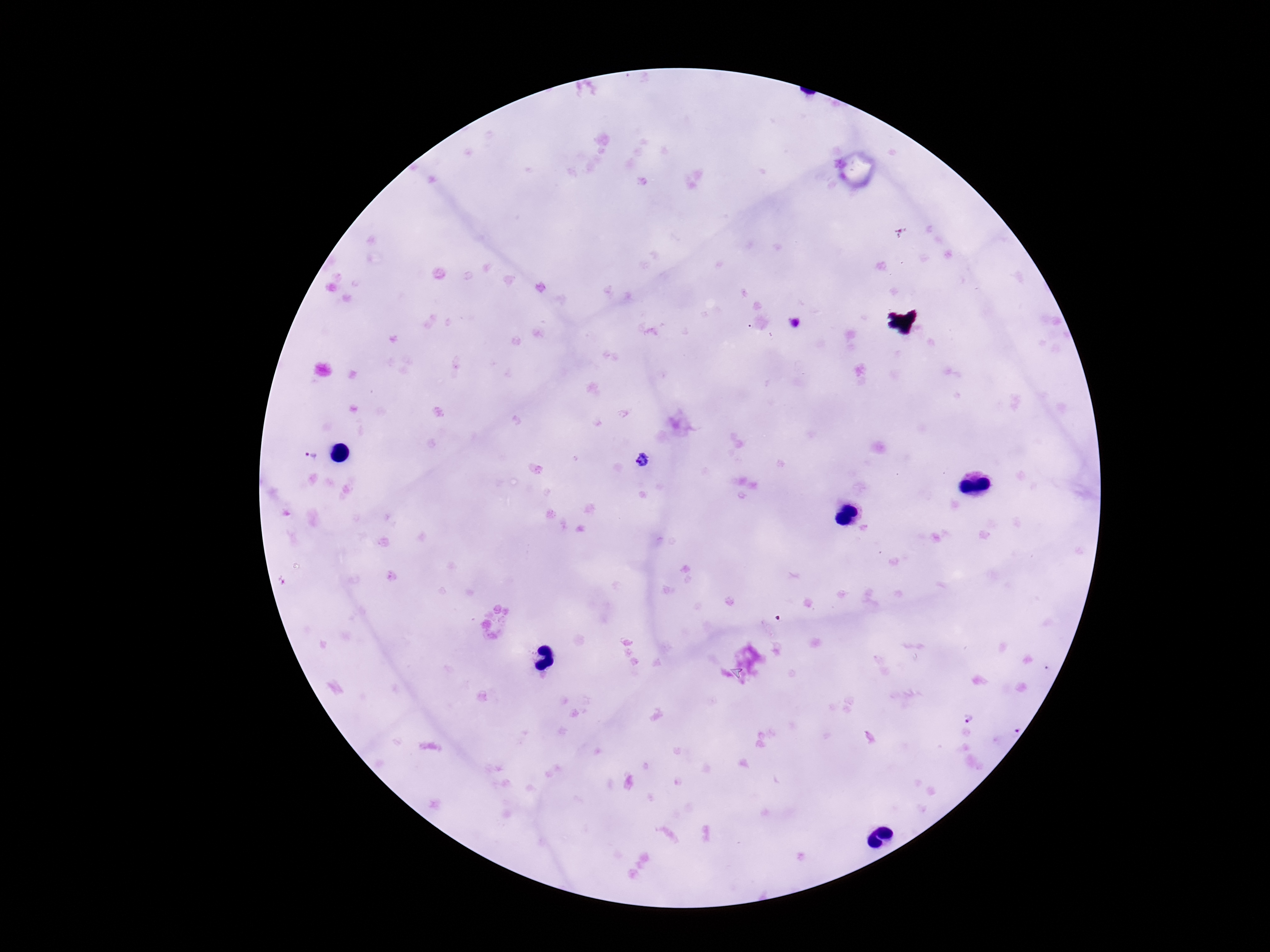
preparation = thick peripheral-blood smear
capture = smartphone camera through the microscope eyepiece
Plasmodium parasite locations = approximate centers as [x, y] in pixels: [796, 323], [309, 456], [641, 459], [968, 717], [1012, 728]
stain = Giemsa
image size = 1270×952 pixels
field of view = one from this slide
patient malaria status = positive
magnification = 100x